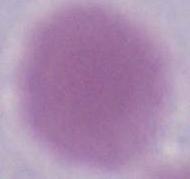
identification = red blood cell
magnification = 1000x
modality = photomicrograph